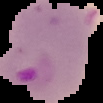

Summary:
  - Image type: cell region segmented out of the field of view; surrounding area masked to black
  - Preparation: thin blood film
  - Result: Plasmodium parasites detected
  - Image size: 103×103 pixels